Give the preparation type.
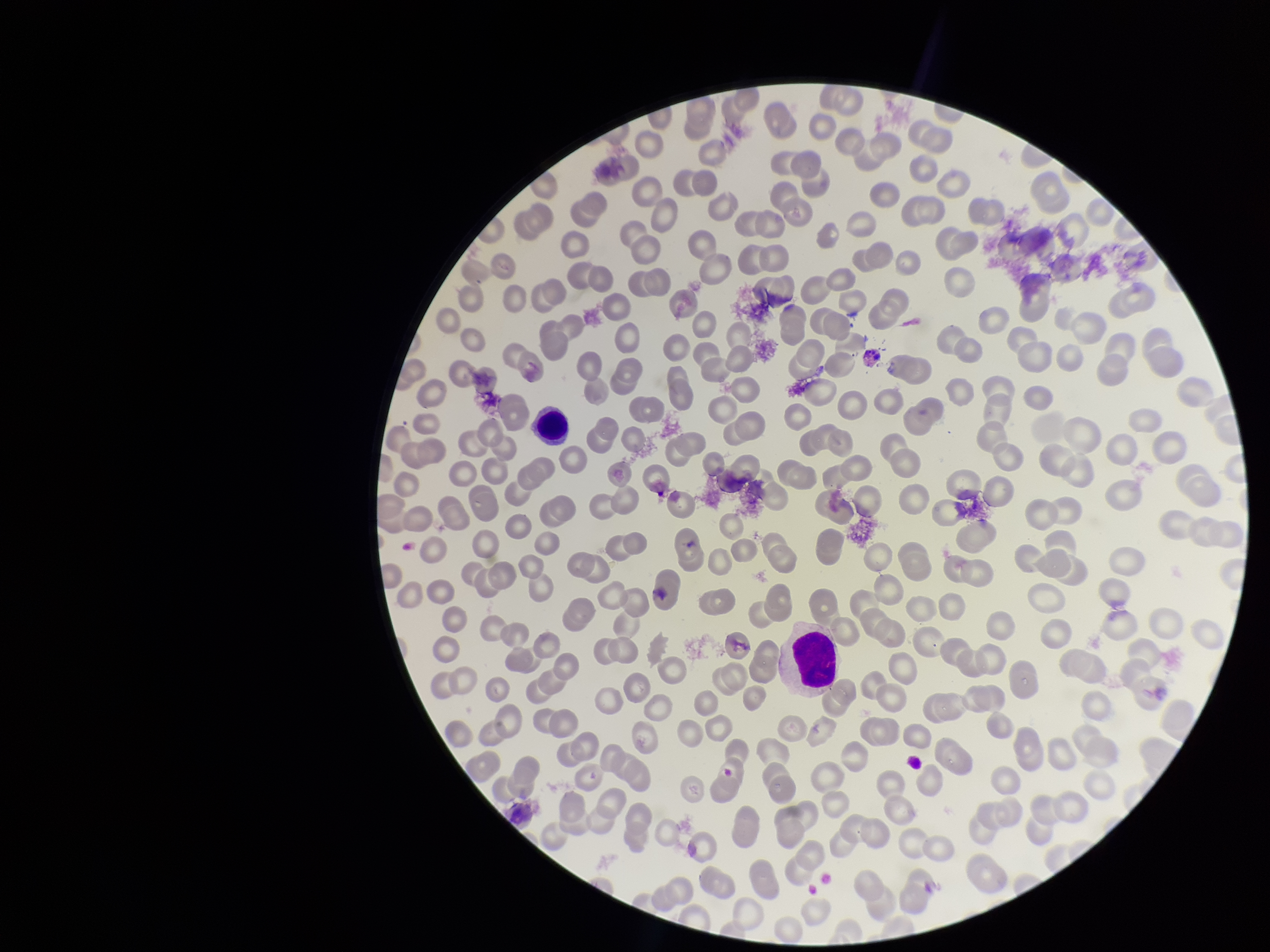

Thin.

Summary:
  - Parasitized red blood cells: none seen
  - Capture: smartphone photograph through the microscope eyepiece
  - Image size: 1270×952 pixels
  - Parasitized red blood cell count: 0
  - Red blood cell count: 225
  - Patient malaria status: negative
  - Stain: Giemsa
  - Field of view: single